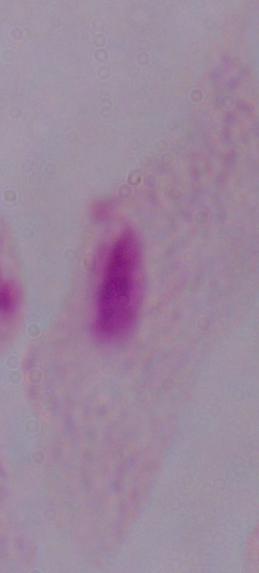

A trichomonad is seen. Micrograph. Captured at 1000x magnification.